Classify this cell by malaria status.
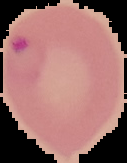

It is parasitized.

Summary:
  - Preparation: thin blood film
  - Image size: 127×163 pixels
  - Image type: segmented cell region on a black background